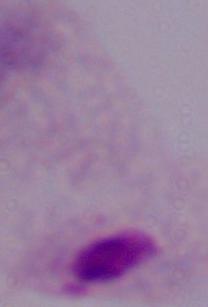

Summary:
  - Identification: trichomonad
  - Modality: micrograph
  - Magnification: 1000x